Report the malaria status of this cell.
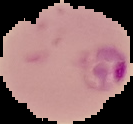

It is parasitized.

Summary:
  - Preparation: thin blood film
  - Image type: segmented cell region with the area outside set to black
  - Image size: 133×124 pixels